Outline each Plasmodium falciparum-infected red blood cell.
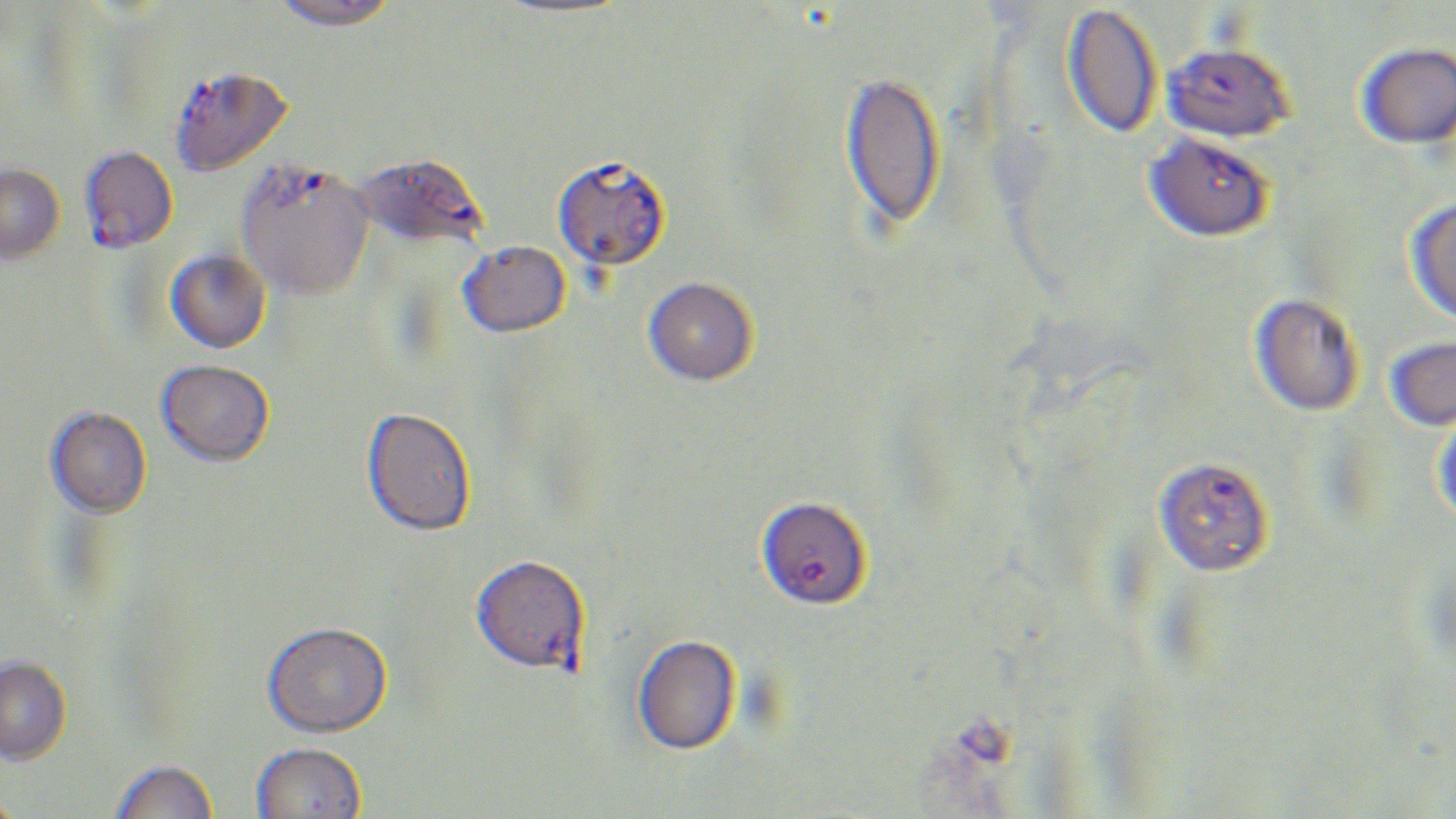

Approximate bounding boxes as [x1, y1, x2, y2] in pixels.
Plasmodium falciparum-infected red blood cells: [1161, 42, 1296, 142], [170, 66, 293, 177], [1144, 130, 1275, 243], [80, 145, 178, 254], [352, 151, 488, 250], [552, 157, 670, 273], [235, 159, 374, 302], [1153, 456, 1274, 577], [760, 502, 869, 608], [471, 558, 590, 677].

{
  "slide_level_diagnosis": "Plasmodium falciparum",
  "modality": "light microscopy",
  "uninfected_red_blood_cell_locations": "approximate bounding boxes as [x1, y1, x2, y2] in pixels: [269, 0, 399, 30], [490, 0, 632, 17], [1061, 3, 1162, 139], [1355, 42, 1456, 149], [839, 71, 946, 232], [0, 162, 65, 264], [1404, 197, 1456, 325], [457, 241, 571, 339], [165, 248, 271, 354], [643, 278, 758, 388], [1249, 293, 1364, 417], [1383, 335, 1456, 432], [155, 360, 274, 467], [45, 407, 152, 519], [361, 408, 476, 538], [1430, 411, 1456, 525], [262, 624, 392, 741], [633, 636, 742, 757], [0, 656, 72, 767], [251, 744, 366, 819], [110, 761, 219, 819]",
  "image_size": "1456×819 pixels",
  "field_of_view": "single",
  "stain": "May-Grünwald-Giemsa",
  "magnification": "1000x",
  "preparation": "thin blood smear"
}